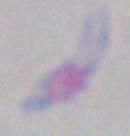

Summary:
  - Magnification: 1000x
  - Identification: Toxoplasma gondii
  - Modality: photomicrograph